Describe the morphology of the erythrocytes.
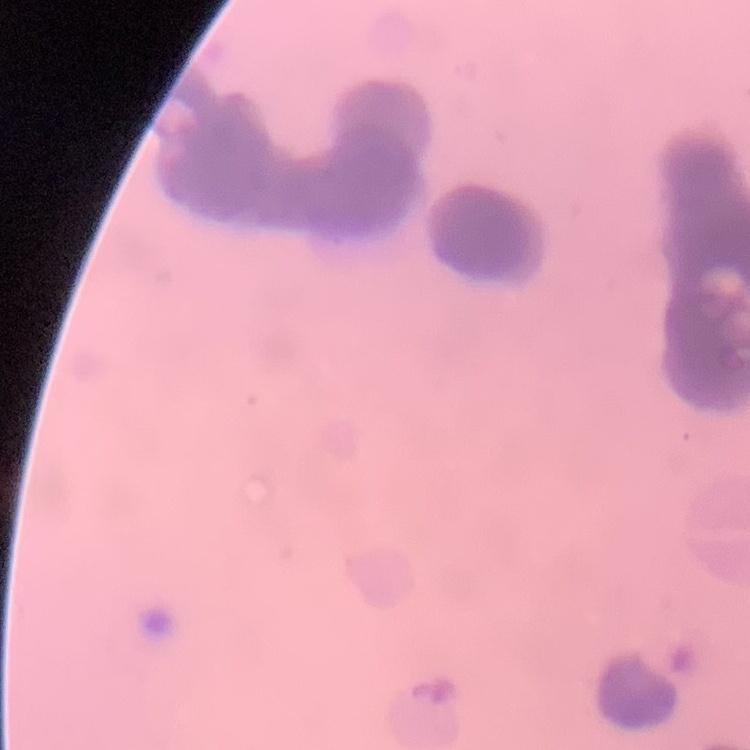
They show rouleaux formation.

Stained with either Field's or Giemsa. Square crop of a larger photomicrograph. Thin peripheral smear.